State which parasite is depicted.
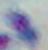
This is Toxoplasma gondii.

Summary:
  - Modality: photomicrograph
  - Magnification: 1000x